Identify the cell.
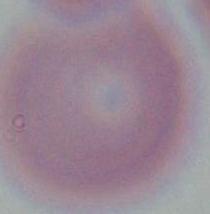

An erythrocyte.

Captured at 1000x magnification. Micrograph.